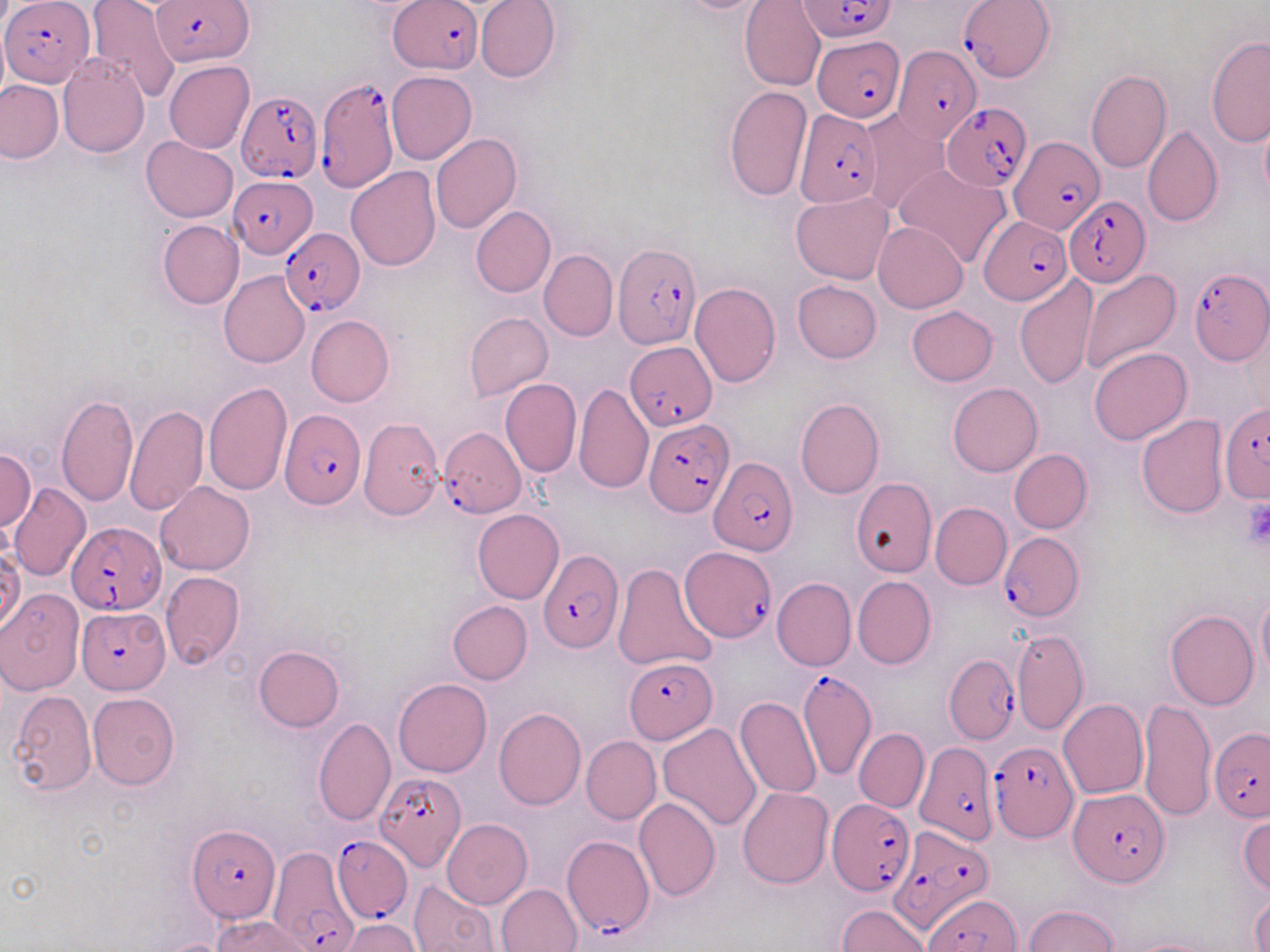 Approximate bounding boxes as [x1, y1, x2, y2] in pixels. Plasmodium falciparum-infected red blood cell locations (subset): [3, 0, 93, 87], [801, 0, 895, 43], [152, 1, 253, 66], [390, 1, 481, 75], [959, 1, 1054, 81], [812, 37, 905, 122], [893, 45, 981, 144], [315, 78, 397, 194], [235, 91, 320, 186], [943, 103, 1032, 191], [794, 108, 880, 207], [1011, 136, 1104, 235], [229, 174, 317, 256], [1065, 197, 1149, 286], [978, 216, 1072, 305], [279, 227, 365, 317], [613, 244, 699, 348], [1188, 268, 1269, 365], [629, 343, 717, 430], [1219, 403, 1270, 506], [279, 412, 366, 511], [644, 416, 732, 517], [439, 426, 525, 516], [708, 455, 799, 555], [66, 521, 166, 614], [997, 533, 1084, 622], [681, 548, 774, 644], [538, 549, 624, 654], [76, 607, 168, 692], [945, 654, 1018, 744], [625, 658, 717, 745], [795, 669, 873, 780], [1210, 726, 1270, 820], [987, 739, 1076, 841], [916, 740, 999, 844], [373, 770, 465, 874], [1069, 787, 1169, 886], [828, 798, 913, 896], [892, 824, 997, 925], [188, 825, 281, 923], [332, 835, 411, 922], [561, 835, 655, 938], [267, 847, 356, 951], [927, 893, 1019, 952]. Platelet locations: [1242, 499, 1270, 551]. Uninfected red blood cell locations (subset): [84, 0, 179, 99], [476, 0, 561, 83], [665, 0, 776, 14], [741, 0, 825, 90], [1205, 35, 1270, 148], [57, 56, 149, 157], [164, 60, 255, 154], [1086, 70, 1172, 173], [386, 71, 477, 164], [0, 80, 64, 164], [724, 85, 812, 204], [858, 110, 949, 215], [1259, 112, 1270, 210], [1143, 124, 1222, 227], [432, 134, 523, 234], [140, 137, 238, 222], [894, 162, 1011, 269], [345, 167, 441, 271], [791, 191, 894, 285], [470, 206, 555, 297], [158, 220, 243, 309], [873, 221, 968, 312], [540, 249, 617, 341], [1080, 269, 1182, 373], [219, 271, 310, 368], [1014, 274, 1097, 393], [792, 280, 881, 363], [689, 283, 780, 387], [907, 306, 998, 386], [464, 312, 553, 401], [307, 315, 394, 406], [1087, 347, 1191, 444], [500, 378, 581, 478], [572, 380, 654, 493], [203, 381, 293, 496], [948, 382, 1042, 476], [56, 393, 138, 507], [795, 397, 885, 498], [125, 404, 208, 517], [1136, 415, 1228, 519], [359, 417, 445, 519], [0, 448, 35, 533], [1009, 448, 1092, 533], [847, 479, 935, 577], [155, 482, 255, 576], [9, 483, 91, 582], [930, 502, 1012, 589], [613, 561, 718, 673], [160, 572, 245, 670], [771, 577, 856, 671], [853, 577, 936, 669], [0, 590, 84, 695], [1256, 591, 1270, 683], [447, 600, 532, 684], [1165, 609, 1259, 710], [1011, 628, 1088, 734], [252, 645, 345, 732], [391, 678, 491, 777], [7, 690, 97, 796], [87, 693, 180, 790], [734, 695, 822, 799], [1138, 697, 1215, 822], [1058, 699, 1148, 800], [492, 707, 586, 810], [313, 718, 396, 826], [657, 722, 762, 830], [853, 728, 928, 812], [581, 736, 661, 825], [737, 787, 833, 888], [634, 797, 721, 900], [1238, 815, 1269, 895], [442, 818, 533, 909], [410, 880, 501, 951], [496, 883, 583, 952], [1250, 891, 1270, 950], [837, 905, 931, 951], [1025, 905, 1118, 952], [213, 915, 318, 952], [343, 918, 420, 951], [1121, 936, 1221, 952]. Slide-level diagnosis: Plasmodium falciparum. Image is 1270×952 pixels. May-Grünwald-Giemsa stain. Thin blood smear. 1000x magnification. One field of a larger specimen. Light microscopy.